Assess this cell for malaria.
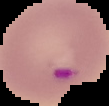

Parasitized.

Image is 109×106 pixels. Cell region segmented out of the field of view; the surrounding area is masked to black. From a thin blood smear.